Locate every blood parasite and identify its species.
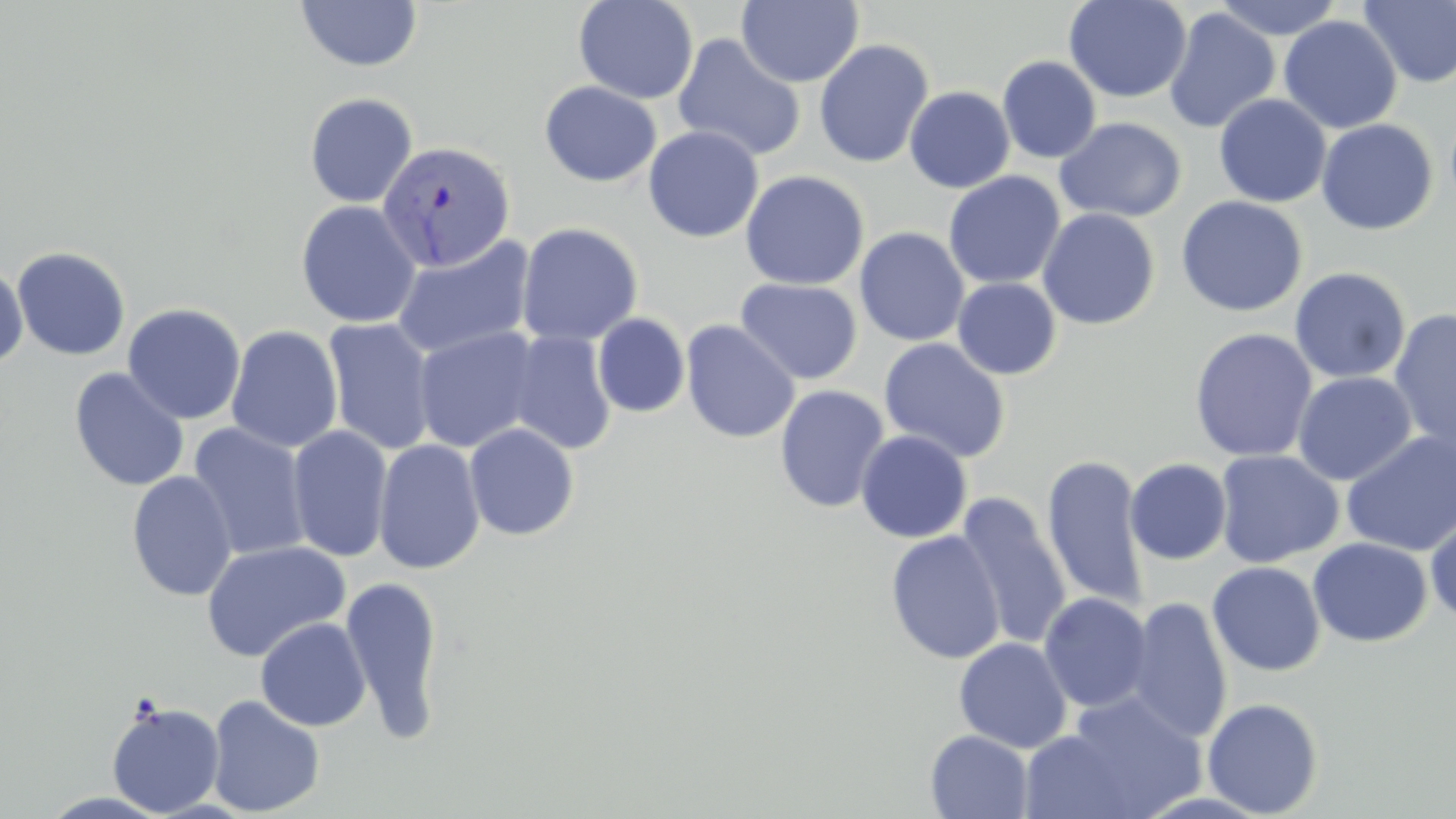
Approximate bounding boxes as named x1/y1/x2/y2 corners in pixels.
Plasmodium vivax-infected red blood cells: (x1=377, y1=140, x2=517, y2=272).
No Plasmodium falciparum, Plasmodium ovale, Plasmodium malariae, Babesia divergens, or Trypanosoma brucei observed.

Uninfected red blood cell locations: (x1=294, y1=0, x2=423, y2=73), (x1=573, y1=0, x2=699, y2=104), (x1=736, y1=0, x2=864, y2=87), (x1=1063, y1=0, x2=1192, y2=103), (x1=1211, y1=0, x2=1345, y2=41), (x1=1357, y1=1, x2=1456, y2=89), (x1=1163, y1=7, x2=1281, y2=134), (x1=1279, y1=15, x2=1402, y2=134), (x1=672, y1=33, x2=807, y2=163), (x1=813, y1=39, x2=934, y2=168), (x1=997, y1=56, x2=1102, y2=164), (x1=539, y1=80, x2=662, y2=187), (x1=904, y1=86, x2=1016, y2=194), (x1=303, y1=92, x2=419, y2=208), (x1=1214, y1=93, x2=1331, y2=208), (x1=1054, y1=116, x2=1187, y2=223), (x1=1316, y1=118, x2=1439, y2=235), (x1=643, y1=126, x2=764, y2=242), (x1=740, y1=170, x2=869, y2=290), (x1=943, y1=171, x2=1065, y2=289), (x1=1176, y1=195, x2=1308, y2=317), (x1=296, y1=200, x2=422, y2=328), (x1=1037, y1=207, x2=1161, y2=330), (x1=517, y1=222, x2=643, y2=346), (x1=854, y1=227, x2=970, y2=346), (x1=392, y1=234, x2=536, y2=360), (x1=11, y1=246, x2=131, y2=360), (x1=0, y1=260, x2=29, y2=371), (x1=1289, y1=267, x2=1412, y2=384), (x1=951, y1=277, x2=1062, y2=379), (x1=735, y1=278, x2=863, y2=385), (x1=122, y1=303, x2=246, y2=425), (x1=1389, y1=307, x2=1456, y2=456), (x1=593, y1=313, x2=690, y2=418), (x1=322, y1=318, x2=438, y2=456), (x1=681, y1=320, x2=800, y2=443), (x1=226, y1=325, x2=343, y2=453), (x1=413, y1=326, x2=542, y2=453), (x1=1189, y1=327, x2=1318, y2=462), (x1=506, y1=331, x2=617, y2=455), (x1=878, y1=337, x2=1011, y2=463), (x1=69, y1=367, x2=189, y2=492), (x1=1292, y1=371, x2=1417, y2=485), (x1=775, y1=384, x2=890, y2=513), (x1=187, y1=422, x2=312, y2=562), (x1=464, y1=422, x2=580, y2=541), (x1=287, y1=425, x2=394, y2=563), (x1=855, y1=429, x2=973, y2=543), (x1=1340, y1=431, x2=1456, y2=555), (x1=373, y1=438, x2=485, y2=575), (x1=1214, y1=450, x2=1344, y2=568), (x1=1041, y1=453, x2=1150, y2=613), (x1=1125, y1=458, x2=1232, y2=565), (x1=126, y1=470, x2=238, y2=602), (x1=1341, y1=480, x2=1456, y2=624), (x1=955, y1=494, x2=1072, y2=651), (x1=1425, y1=509, x2=1456, y2=625), (x1=885, y1=530, x2=1006, y2=664), (x1=1308, y1=537, x2=1433, y2=646), (x1=200, y1=540, x2=351, y2=662), (x1=1207, y1=562, x2=1326, y2=677), (x1=341, y1=574, x2=445, y2=740), (x1=1039, y1=592, x2=1154, y2=713), (x1=1124, y1=596, x2=1233, y2=744), (x1=255, y1=617, x2=371, y2=732), (x1=954, y1=637, x2=1073, y2=753), (x1=1056, y1=692, x2=1206, y2=817), (x1=207, y1=695, x2=325, y2=816), (x1=1201, y1=697, x2=1324, y2=817), (x1=106, y1=701, x2=225, y2=817), (x1=1017, y1=729, x2=1143, y2=819), (x1=925, y1=730, x2=1034, y2=818). Slide-level diagnosis: Plasmodium vivax. One field of a larger specimen. Light microscopy. Thin blood smear. May-Grünwald-Giemsa stain. 1000x magnification. Image is 1456×819 pixels.